Classify this cell by malaria status.
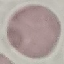

It is uninfected.

preparation = thin blood film
capture = smartphone through the microscope eyepiece
stain = Giemsa
image type = cell patch, automatically extracted from a larger field of view and resized to 64 × 64 pixels